Report the malaria status of this cell.
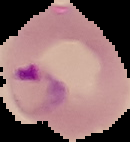
It is parasitized.

Summary:
  - Preparation: thin blood film
  - Image size: 130×142 pixels
  - Image type: segmented cell region on a black background